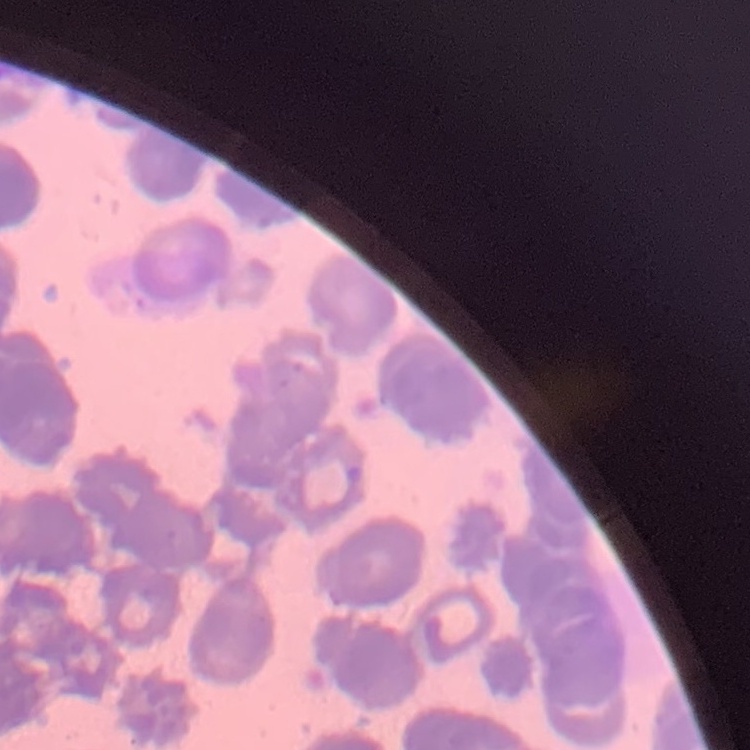
red_blood_cell_morphology: rouleaux formation
image_type: square crop of a larger photomicrograph
stain: Field's or Giemsa
preparation: thin blood smear